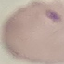
Summary:
  - Result: malaria parasites detected
  - Stain: Giemsa
  - Image type: automatically extracted cell patch, resized to 64 × 64 pixels
  - Capture: smartphone camera at the microscope eyepiece
  - Preparation: thin blood film